Locate and identify every blood parasite.
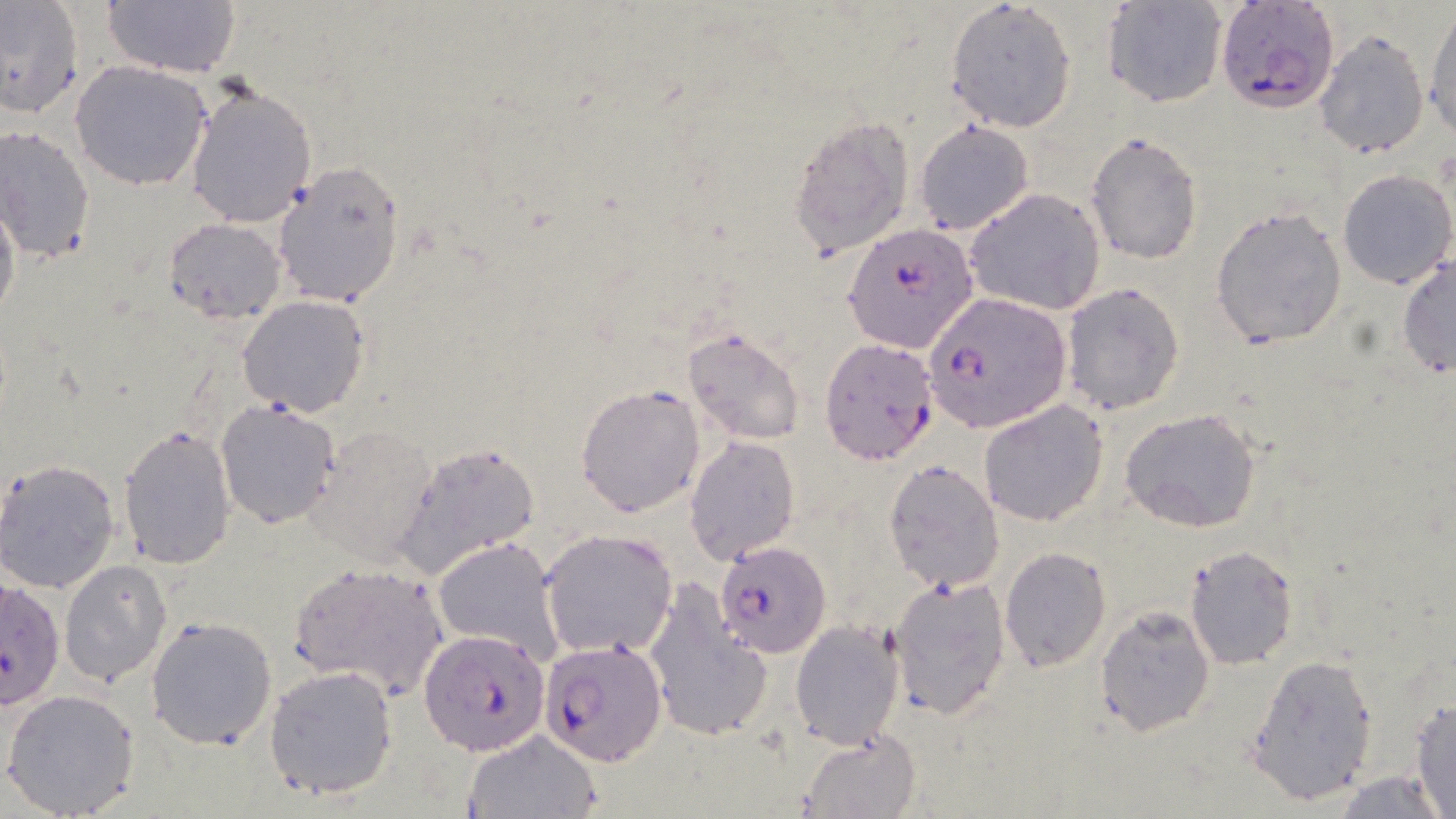

Approximate bounding boxes as (x1, y1, x2, y2) in pixels.
Plasmodium falciparum-infected red blood cells: (1214, 1, 1338, 112), (844, 221, 979, 354), (923, 291, 1071, 432), (820, 337, 942, 468), (714, 542, 833, 657), (0, 579, 59, 716), (423, 627, 551, 755), (539, 638, 668, 765).
No Plasmodium ovale, Plasmodium malariae, Plasmodium vivax, Babesia divergens, or Trypanosoma brucei observed.

Uninfected red blood cell locations: (0, 0, 85, 119), (100, 0, 242, 80), (1103, 0, 1227, 109), (943, 1, 1077, 133), (1425, 8, 1456, 140), (1314, 30, 1429, 159), (70, 60, 213, 190), (186, 80, 317, 229), (789, 113, 916, 258), (914, 122, 1032, 235), (0, 125, 95, 266), (1086, 133, 1203, 265), (273, 163, 406, 308), (1336, 168, 1455, 289), (966, 188, 1106, 316), (0, 192, 20, 329), (1210, 205, 1348, 351), (164, 217, 288, 322), (1397, 256, 1455, 378), (1060, 284, 1184, 416), (237, 295, 370, 418), (681, 325, 806, 446), (575, 384, 706, 518), (215, 399, 342, 530), (978, 400, 1108, 525), (1120, 407, 1261, 532), (308, 422, 439, 567), (117, 425, 237, 570), (685, 435, 801, 565), (395, 442, 542, 580), (1, 459, 122, 592), (881, 459, 1004, 593), (539, 529, 679, 659), (432, 536, 567, 667), (1184, 544, 1298, 670), (998, 546, 1112, 672), (60, 560, 172, 686), (287, 560, 450, 700), (888, 574, 1013, 720), (644, 580, 770, 743), (1095, 606, 1214, 736), (146, 615, 278, 752), (790, 619, 905, 751), (1246, 652, 1378, 806), (262, 664, 401, 800), (2, 688, 142, 818), (1409, 698, 1456, 819), (801, 728, 922, 818), (465, 731, 600, 818), (1329, 771, 1451, 818). Slide-level diagnosis: Plasmodium falciparum. Light microscopy. May-Grünwald-Giemsa stain. 1000x magnification. One field of a larger specimen. Image is 1456×819 pixels. Thin blood smear.